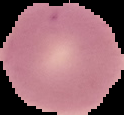

{
  "preparation": "thin blood smear",
  "image_type": "segmented cell region with the area outside set to black",
  "image_size": "124×115 pixels",
  "result": "no malaria parasites seen"
}